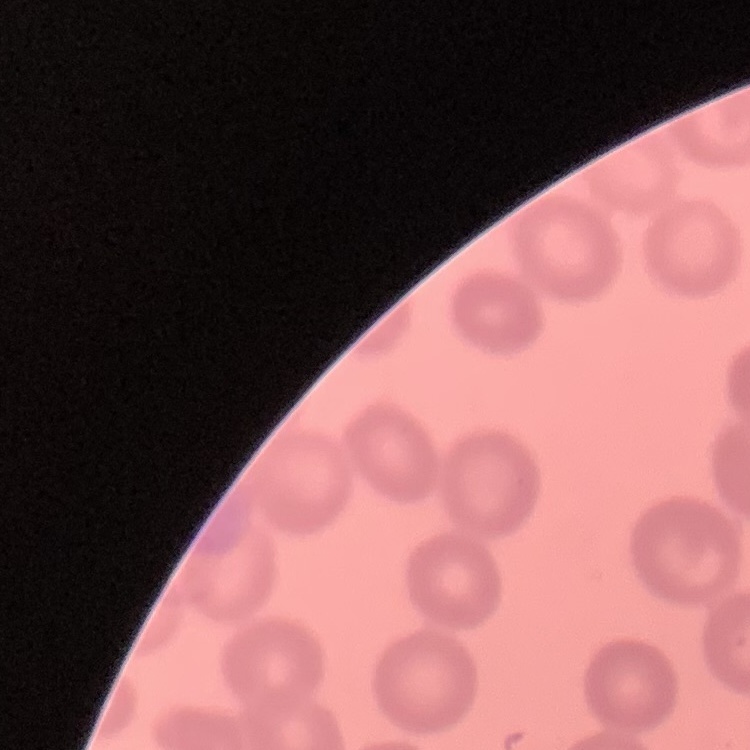
erythrocyte morphology = no rouleaux formation
preparation = thin peripheral smear
stain = Field's or Giemsa
image type = one tile cut from a larger photomicrograph